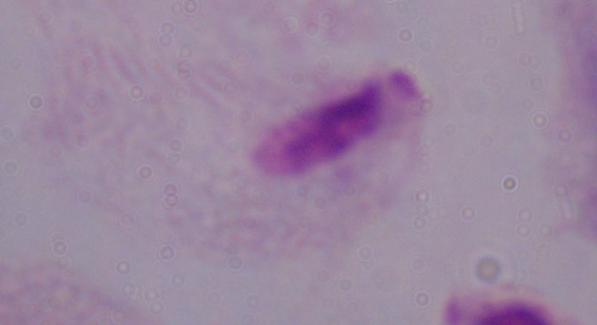

Summary:
  - Identification: trichomonad
  - Modality: photomicrograph
  - Magnification: 1000x